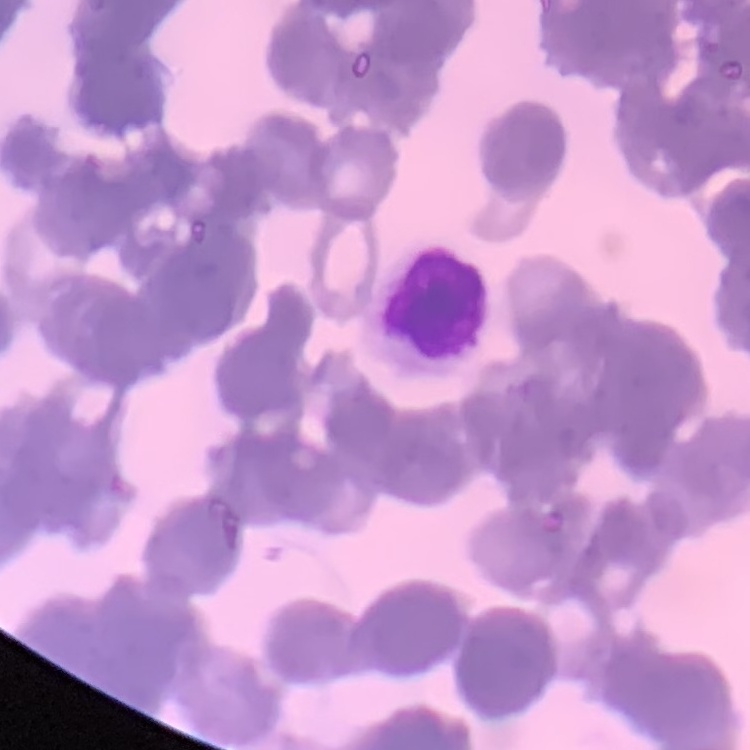

The erythrocytes show rouleaux formation. Stained with either Field's or Giemsa. Thin blood film. One tile cut from a larger photomicrograph.